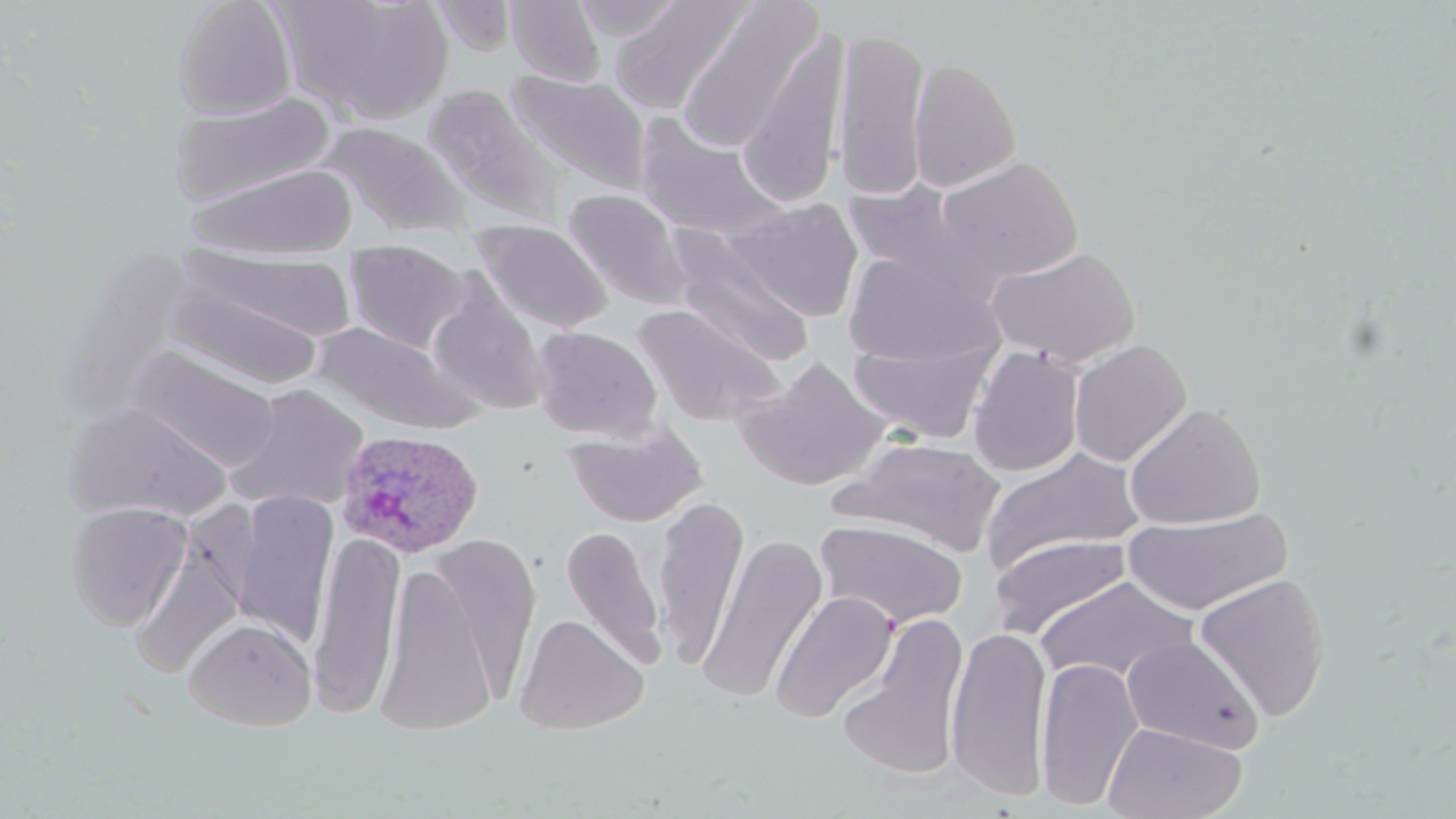
Approximate bounding boxes as [x1, y1, x2, y2] in pixels. Plasmodium ovale-infected red blood cell locations: [336, 429, 484, 558]. Uninfected red blood cell locations: [171, 0, 297, 120], [281, 0, 455, 125], [506, 0, 605, 86], [571, 0, 684, 41], [610, 0, 750, 113], [677, 1, 822, 151], [737, 26, 849, 205], [831, 26, 930, 202], [908, 57, 1021, 192], [506, 70, 651, 195], [423, 84, 566, 227], [169, 91, 335, 207], [633, 112, 786, 243], [318, 122, 473, 236], [934, 157, 1083, 285], [187, 163, 358, 261], [841, 182, 970, 281], [562, 187, 695, 310], [729, 198, 864, 322], [473, 218, 612, 335], [668, 231, 815, 368], [344, 239, 471, 354], [985, 245, 1141, 369], [183, 247, 358, 345], [843, 251, 999, 369], [425, 276, 550, 415], [167, 277, 328, 390], [633, 305, 784, 428], [307, 320, 486, 435], [530, 325, 663, 442], [847, 338, 996, 445], [1069, 340, 1192, 467], [967, 345, 1084, 477], [129, 346, 281, 472], [736, 357, 890, 490], [226, 384, 369, 511], [64, 400, 231, 523], [1124, 402, 1266, 529], [564, 423, 707, 527], [834, 437, 1007, 556], [982, 448, 1143, 572], [230, 491, 338, 645], [652, 495, 749, 671], [65, 501, 192, 631], [1123, 508, 1292, 617], [814, 518, 967, 630], [560, 525, 667, 667], [308, 529, 405, 717], [422, 533, 542, 704], [698, 533, 828, 705], [990, 534, 1133, 638], [131, 545, 243, 679], [375, 561, 498, 734], [1194, 573, 1331, 722], [1035, 576, 1199, 687], [770, 591, 898, 723], [513, 613, 649, 734], [837, 615, 971, 784], [184, 617, 316, 730], [945, 625, 1053, 801], [1122, 635, 1264, 755], [1035, 656, 1145, 811], [1102, 722, 1248, 819]. Slide-level diagnosis: Plasmodium ovale. May-Grünwald-Giemsa-stained preparation. Image is 1456×819 pixels. Light microscopy. Single field of view. Thin blood film. Captured at 1000x magnification.